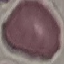

{
  "malaria_status": "uninfected",
  "preparation": "thin blood film",
  "image_type": "cell patch, automatically extracted from a larger field of view and resized to 64 × 64 pixels",
  "capture": "smartphone through the microscope eyepiece",
  "stain": "Giemsa"
}